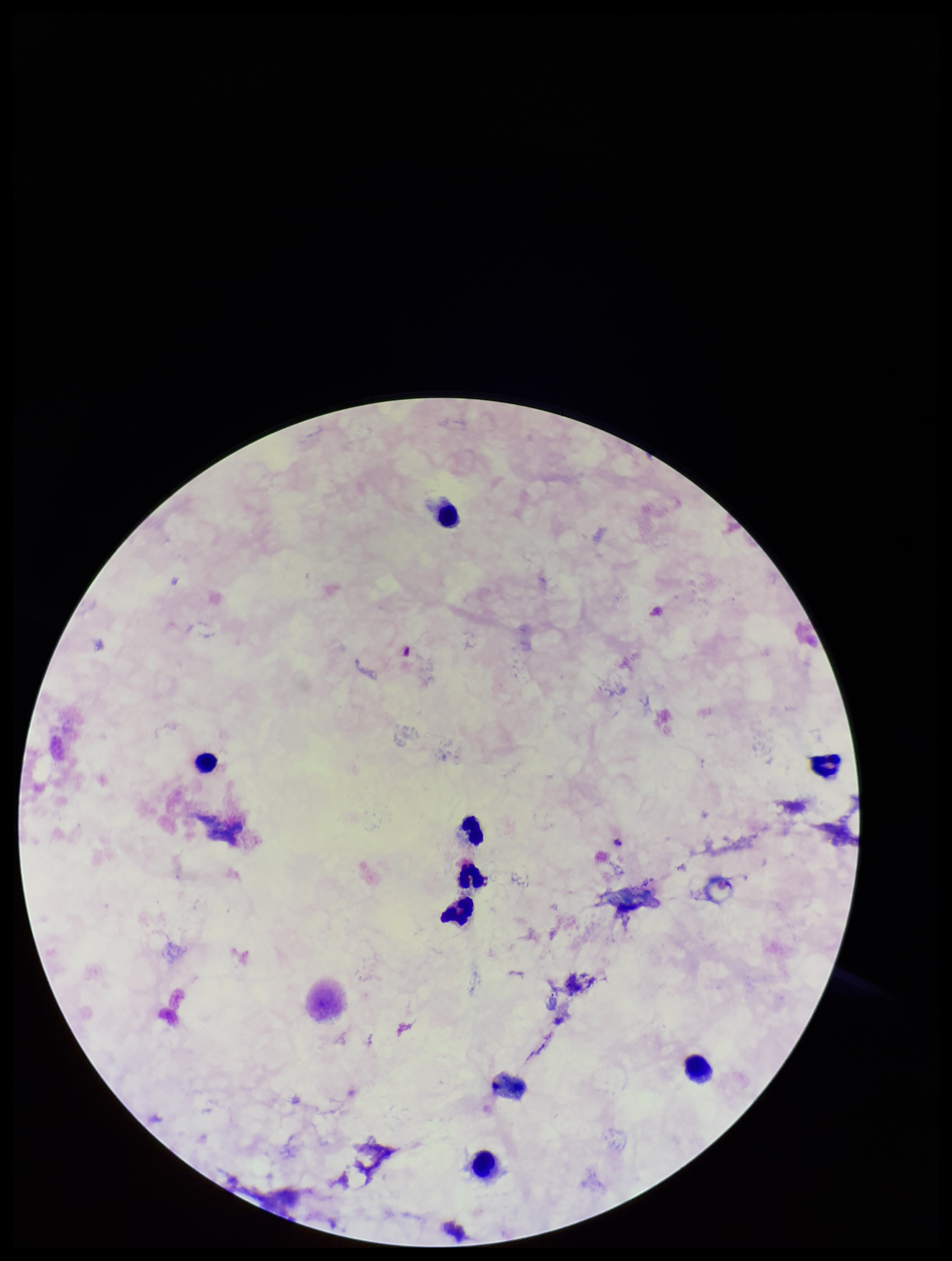
Plasmodium parasites = none identified
parasite count = 0
leukocyte count = 9
preparation = thick smear
capture = smartphone photograph through the microscope eyepiece
patient malaria status = infected
field of view = single
species reported for this patient = Plasmodium falciparum
image size = 952×1261 pixels
stain = Giemsa